Name the parasite shown.
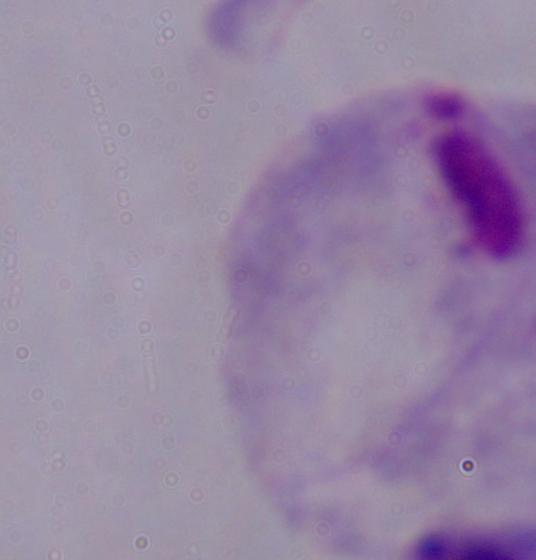
This is a trichomonad.

Summary:
  - Modality: micrograph
  - Magnification: 1000x